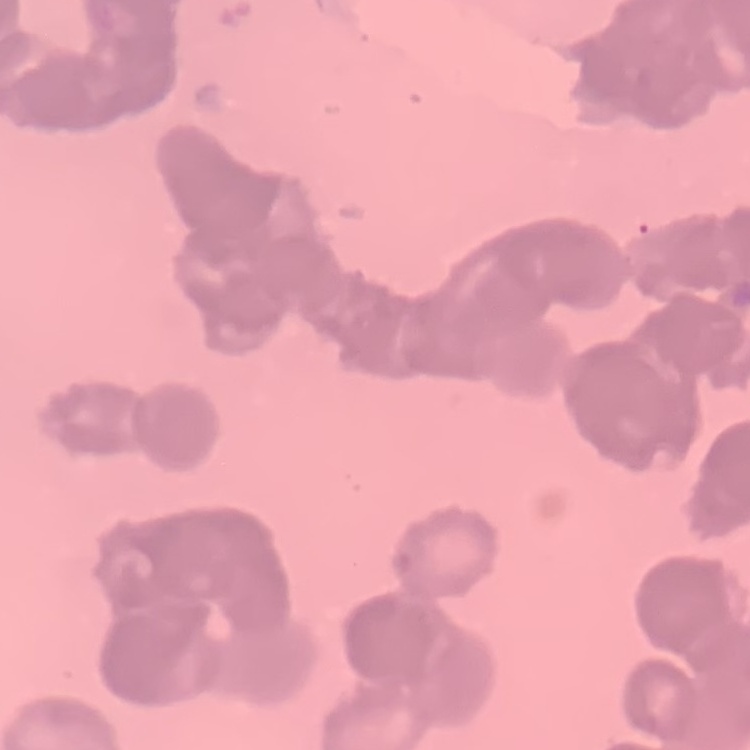

Summary:
  - Red blood cell morphology: rouleaux formation
  - Image type: one tile cut from a larger photomicrograph
  - Preparation: thin peripheral smear
  - Stain: Field's or Giemsa